Assess the morphology of the red blood cells.
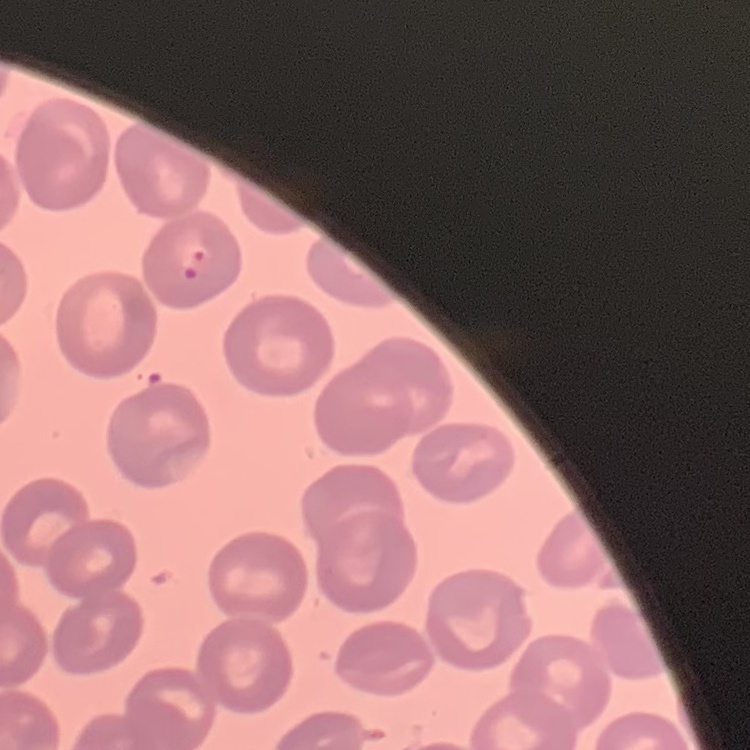

No rouleaux formation.

Field's or Giemsa stain. Thin blood film. One tile cut from a larger photomicrograph.